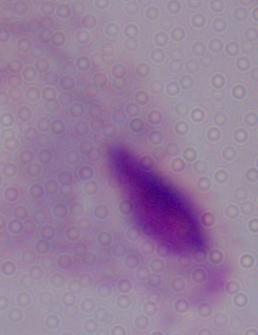 1000x magnification. Photomicrograph. A trichomonad is seen.